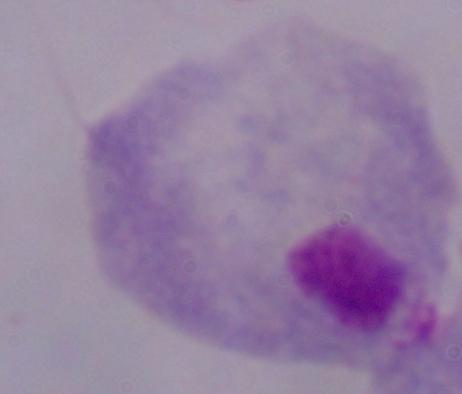

A trichomonad is seen. Photomicrograph. Captured at 1000x magnification.